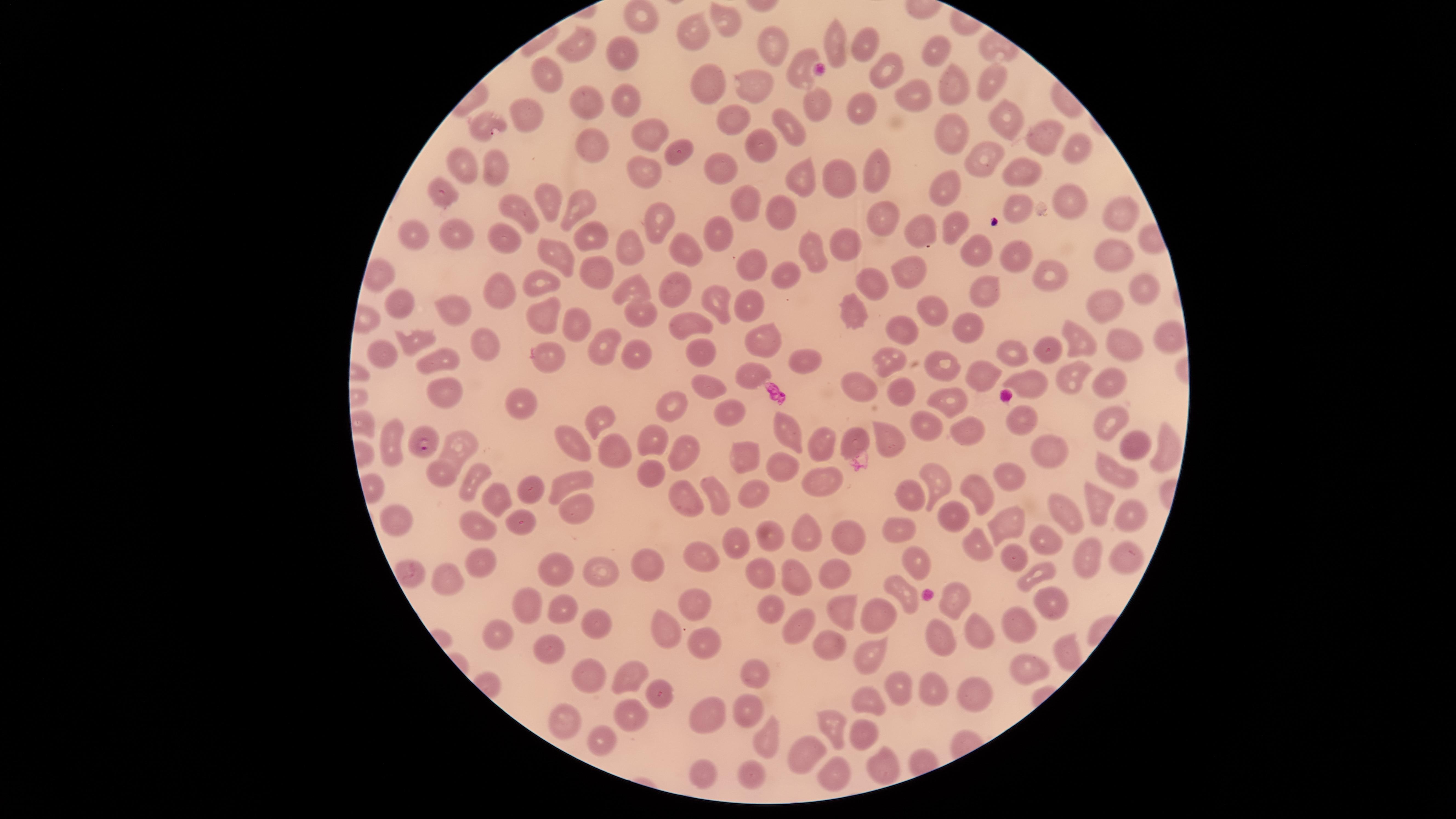
Approximate marker points as [x, y] in pixels. Parasitized RBCs: [421, 444]. Uninfected RBCs: [642, 16], [728, 19], [696, 30], [835, 40], [859, 42], [581, 44], [776, 45], [932, 48], [618, 55], [800, 65], [545, 70], [882, 73], [706, 81], [951, 82], [990, 83], [756, 87], [910, 92], [624, 95], [822, 102], [586, 106], [533, 115], [860, 115], [997, 115], [732, 119], [481, 122], [793, 127], [647, 130], [1032, 132], [949, 135], [758, 141], [589, 143], [1076, 148], [681, 150], [983, 157], [460, 158], [720, 165], [498, 166], [641, 166], [875, 167], [836, 173], [1028, 173], [801, 174], [943, 183], [442, 190], [1071, 193], [553, 198], [745, 199], [777, 203], [1021, 204], [574, 206], [521, 209], [1116, 211], [657, 216], [952, 217], [882, 219], [919, 231], [590, 232], [410, 233], [463, 233], [712, 236], [506, 239], [843, 241], [636, 244], [680, 245], [807, 248], [1111, 250], [984, 252], [551, 253], [1023, 255], [752, 260], [595, 267], [910, 268], [794, 270], [374, 274], [1053, 276], [546, 282], [871, 282], [1141, 284], [984, 286], [667, 287], [631, 288], [713, 288], [496, 290], [1097, 300], [399, 301], [461, 304], [747, 304], [641, 309], [851, 310], [934, 310], [536, 312], [578, 323], [697, 323], [959, 323], [892, 332], [759, 333], [1162, 333], [412, 337], [1081, 338], [481, 341], [1128, 344], [599, 346], [383, 348], [1043, 350], [704, 351], [548, 353], [1006, 354], [644, 355], [437, 358], [808, 358], [883, 360], [944, 365], [753, 370], [1071, 373], [984, 374], [1027, 377], [857, 379], [1111, 380], [712, 387], [899, 387], [447, 390], [949, 395], [673, 400], [517, 401], [594, 412], [727, 412], [1019, 417], [1112, 421], [931, 424], [786, 425], [968, 432], [462, 433], [654, 433], [570, 435], [894, 435], [858, 439], [390, 442], [684, 446], [819, 446], [619, 447], [1043, 447], [1135, 447], [744, 449], [1163, 449], [448, 459], [786, 464], [1013, 471], [575, 474], [936, 474], [1113, 474], [442, 475], [651, 475], [472, 477], [816, 481], [529, 488], [751, 490], [917, 491], [978, 492], [686, 497], [499, 498], [720, 498], [1101, 500], [577, 508], [1067, 509], [1125, 511], [957, 512], [395, 515], [1004, 520], [522, 523], [477, 526], [902, 527], [806, 528], [770, 534], [1048, 538], [735, 539], [851, 540], [981, 541], [1131, 554], [913, 555], [1017, 555], [1089, 556], [644, 557], [695, 557], [477, 563], [600, 563], [559, 564], [829, 564], [411, 569], [756, 570], [1040, 572], [790, 573], [448, 577], [899, 583], [1043, 596], [693, 599], [955, 599], [838, 602], [531, 604], [568, 606], [774, 606], [1019, 611], [882, 612], [594, 621], [666, 625], [978, 625], [799, 627], [492, 633], [936, 634], [698, 635], [551, 643], [823, 644], [1061, 647], [867, 653], [1022, 668], [585, 669], [634, 670], [749, 670], [896, 684], [933, 690], [969, 692], [658, 694], [869, 700], [747, 703], [626, 710], [561, 717], [704, 717], [833, 723], [863, 732], [766, 733], [607, 736], [801, 749], [882, 767], [704, 770], [750, 770], [835, 774]. Smartphone photograph through the microscope eyepiece. Image is 1456×819 pixels. Giemsa-stained preparation. Presence: malaria parasites seen. Species: Plasmodium falciparum. Single field of view. Thin blood film. The visible region is circular.